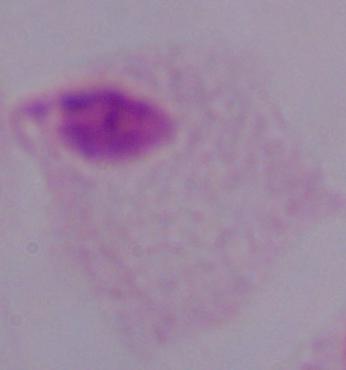 A trichomonad is shown. Photomicrograph. Captured at 1000x magnification.